Assess the morphology of the red blood cells.
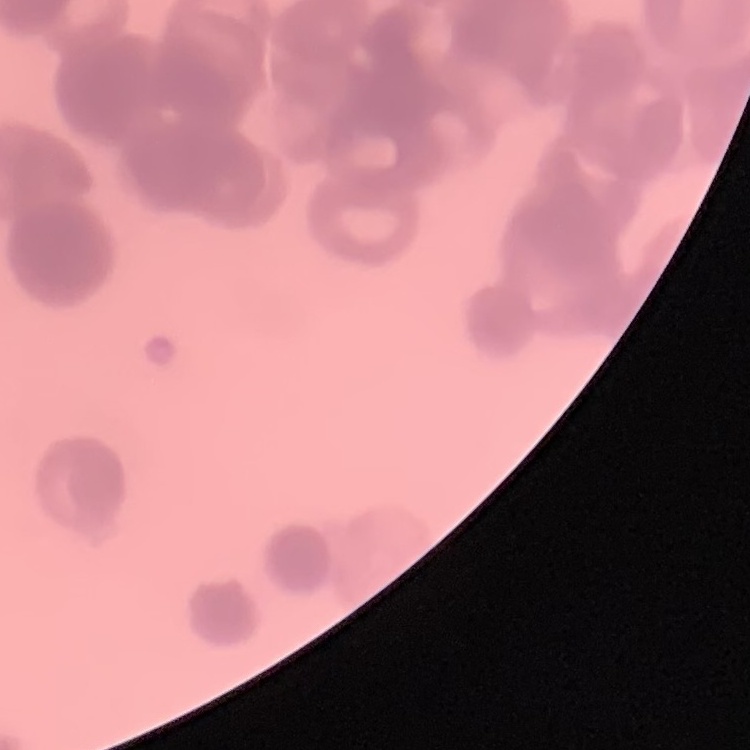
Rouleaux formation.

stain: Field's or Giemsa
image_type: one tile cut from a larger photomicrograph
preparation: thin blood smear